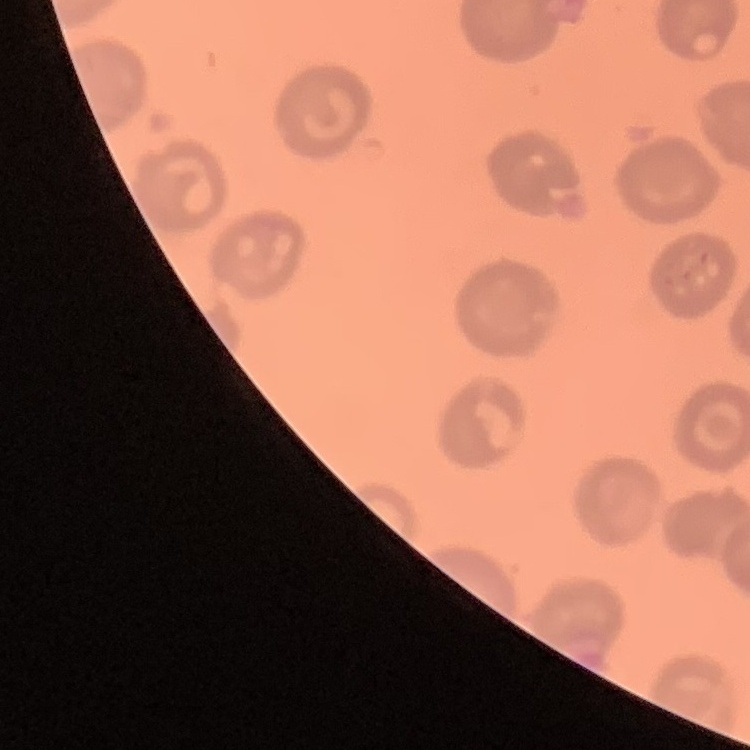 The erythrocytes show no rouleaux formation. Square crop of a larger photomicrograph. Thin blood film. Field's or Giemsa stain.